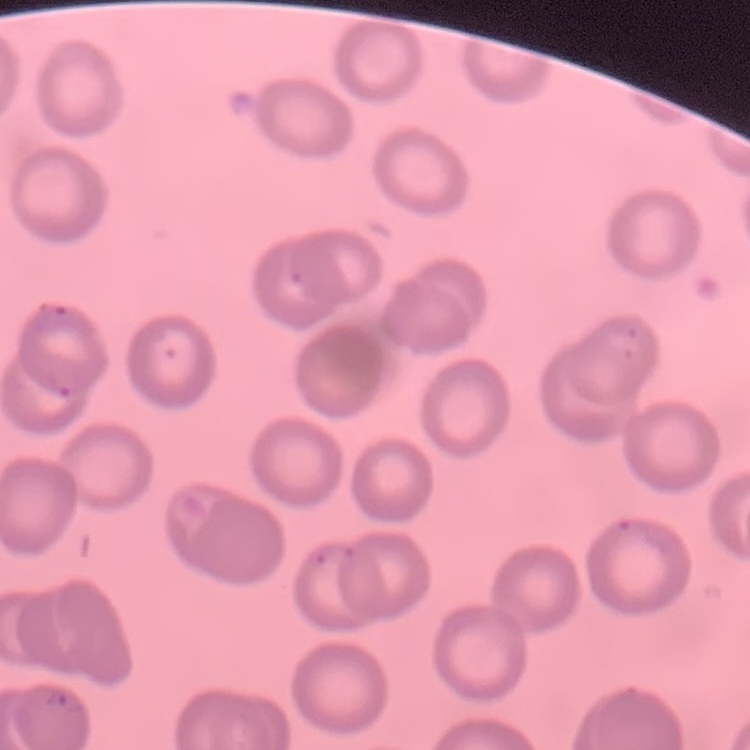 The erythrocytes show no rouleaux formation. Thin peripheral smear. One tile cut from a larger photomicrograph. Field's or Giemsa stain.